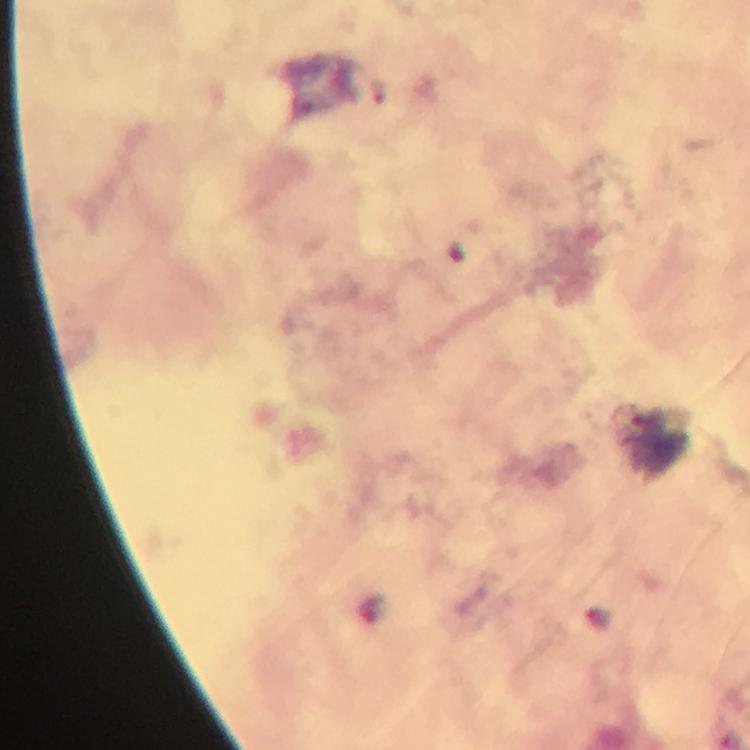
Approximate centers as {x, y} in pixels. Malaria parasite locations: {378, 91}. Smartphone photograph taken through a microscope. Thick blood film. Immersion oil applied. Giemsa stain. Image is 750×750 pixels. From a diagnostic examination for malaria. A crop from one field of view. 100x magnification.